Name the parasite shown.
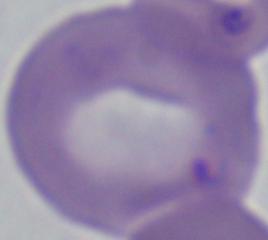
This is Babesia.

Photomicrograph. Captured at 1000x magnification.